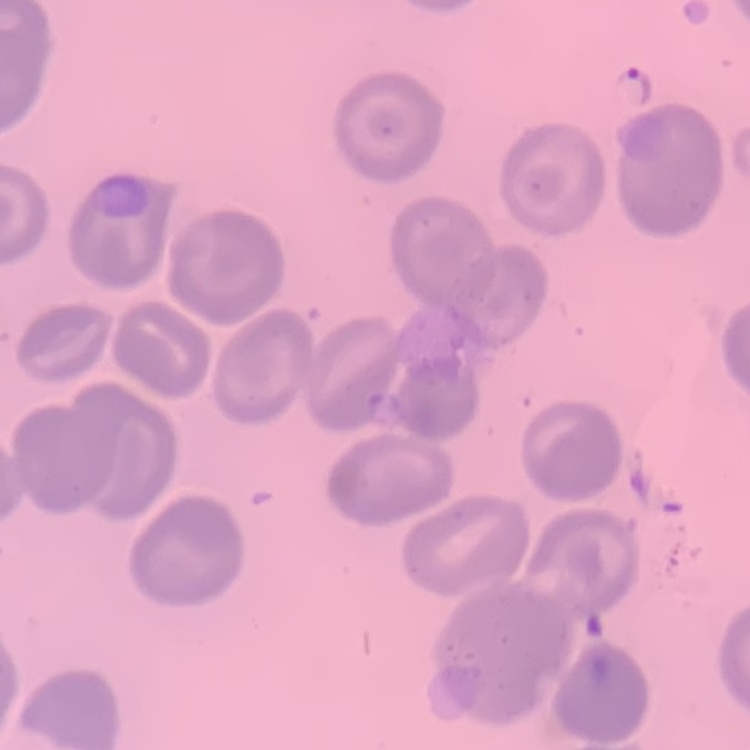

erythrocyte morphology = no rouleaux formation
preparation = thin peripheral smear
image type = one tile cut from a larger photomicrograph
stain = Field's or Giemsa